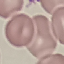
Malaria status: uninfected. Cell patch, automatically extracted from a larger field of view and resized to 64 × 64 pixels. Thin blood smear. Photographed with a smartphone camera at the microscope eyepiece. Giemsa-stained preparation.